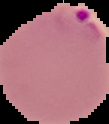
{
  "image_type": "cell region segmented out of the field of view; surrounding area masked to black",
  "result": "Plasmodium parasites identified",
  "preparation": "thin blood film",
  "image_size": "109×124 pixels"
}